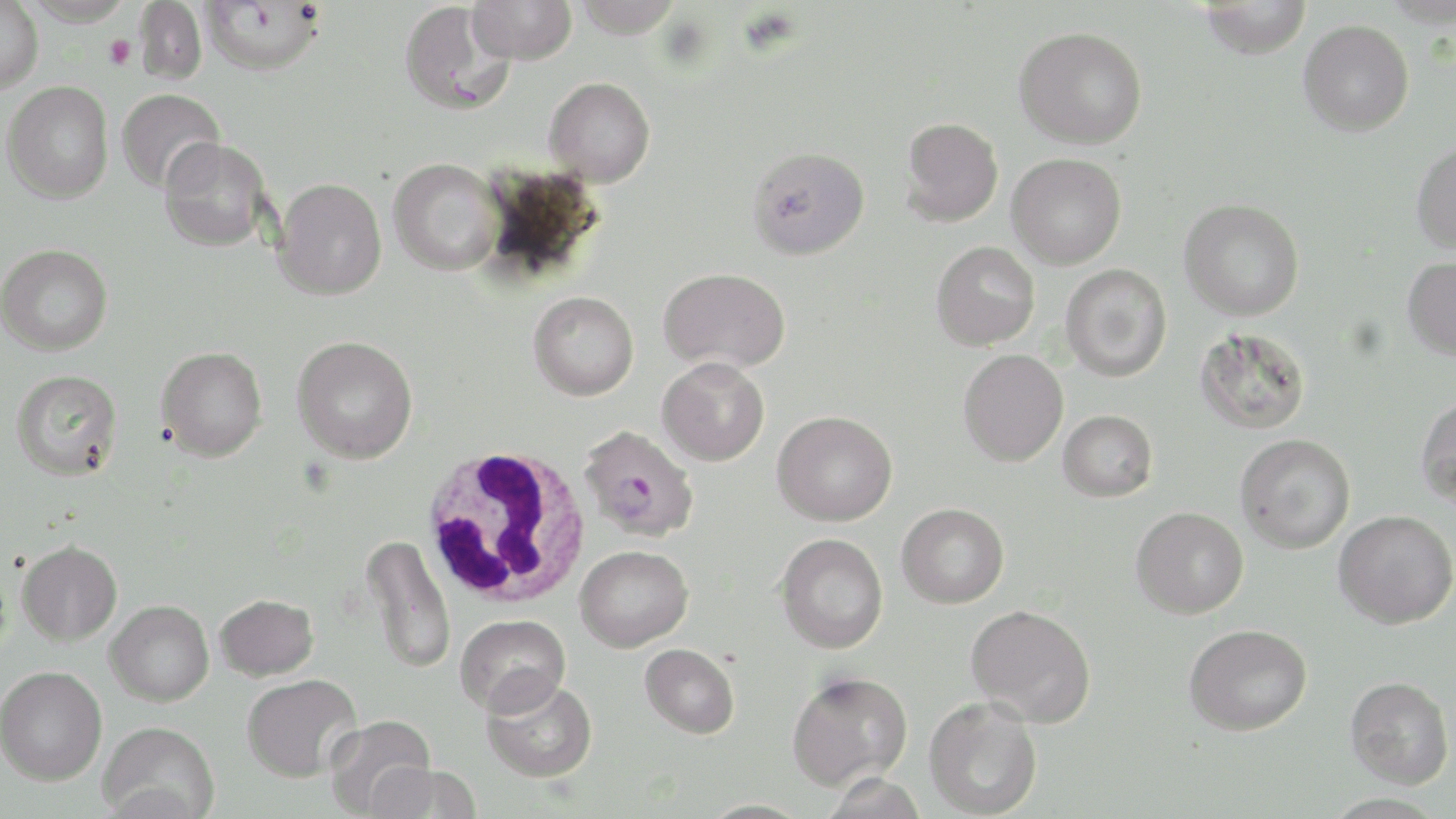 Approximate bounding boxes as named x1/y1/x2/y2 corners in pixels. Plasmodium falciparum-infected red blood cell locations: (x1=579, y1=424, x2=699, y2=542). Uninfected red blood cell locations: (x1=201, y1=0, x2=325, y2=74), (x1=467, y1=0, x2=576, y2=65), (x1=572, y1=0, x2=685, y2=38), (x1=0, y1=1, x2=44, y2=93), (x1=135, y1=1, x2=207, y2=84), (x1=1198, y1=1, x2=1313, y2=59), (x1=400, y1=2, x2=515, y2=116), (x1=1298, y1=20, x2=1414, y2=136), (x1=1013, y1=26, x2=1148, y2=149), (x1=544, y1=76, x2=655, y2=187), (x1=2, y1=81, x2=113, y2=204), (x1=116, y1=88, x2=226, y2=193), (x1=900, y1=117, x2=1003, y2=226), (x1=159, y1=136, x2=272, y2=252), (x1=1410, y1=141, x2=1456, y2=254), (x1=748, y1=146, x2=870, y2=260), (x1=1007, y1=153, x2=1127, y2=269), (x1=388, y1=158, x2=503, y2=275), (x1=273, y1=177, x2=386, y2=300), (x1=1179, y1=199, x2=1305, y2=321), (x1=931, y1=241, x2=1040, y2=350), (x1=0, y1=243, x2=113, y2=355), (x1=1402, y1=256, x2=1456, y2=360), (x1=1060, y1=263, x2=1172, y2=381), (x1=658, y1=267, x2=790, y2=374), (x1=528, y1=291, x2=639, y2=400), (x1=1194, y1=326, x2=1311, y2=434), (x1=291, y1=335, x2=418, y2=463), (x1=156, y1=346, x2=268, y2=461), (x1=958, y1=350, x2=1068, y2=466), (x1=657, y1=357, x2=770, y2=466), (x1=10, y1=369, x2=123, y2=481), (x1=1415, y1=393, x2=1456, y2=509), (x1=772, y1=410, x2=897, y2=526), (x1=1058, y1=410, x2=1158, y2=502), (x1=1235, y1=433, x2=1356, y2=553), (x1=897, y1=503, x2=1009, y2=608), (x1=1131, y1=506, x2=1248, y2=619), (x1=1333, y1=509, x2=1456, y2=628), (x1=360, y1=533, x2=456, y2=674), (x1=776, y1=533, x2=888, y2=654), (x1=17, y1=540, x2=122, y2=646), (x1=575, y1=545, x2=693, y2=652), (x1=214, y1=593, x2=318, y2=681), (x1=105, y1=600, x2=214, y2=706), (x1=966, y1=604, x2=1096, y2=728), (x1=455, y1=613, x2=570, y2=716), (x1=1184, y1=623, x2=1312, y2=735), (x1=639, y1=643, x2=740, y2=738), (x1=0, y1=665, x2=107, y2=785), (x1=786, y1=669, x2=913, y2=791), (x1=241, y1=674, x2=362, y2=782), (x1=481, y1=675, x2=597, y2=783), (x1=1345, y1=675, x2=1454, y2=788), (x1=924, y1=696, x2=1042, y2=818), (x1=322, y1=715, x2=436, y2=817), (x1=98, y1=720, x2=219, y2=819), (x1=368, y1=762, x2=482, y2=819), (x1=822, y1=772, x2=928, y2=818). Platelet locations: (x1=104, y1=35, x2=136, y2=69). White blood cell locations: (x1=420, y1=446, x2=591, y2=612). Slide-level diagnosis: Plasmodium falciparum. One field of a larger specimen. May-Grünwald-Giemsa stain. Light microscopy. 1000x magnification. Image is 1456×819 pixels. Thin blood smear.